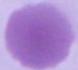
magnification = 1000x
identification = erythrocyte
modality = photomicrograph